Outline each Plasmodium malariae-infected red blood cell.
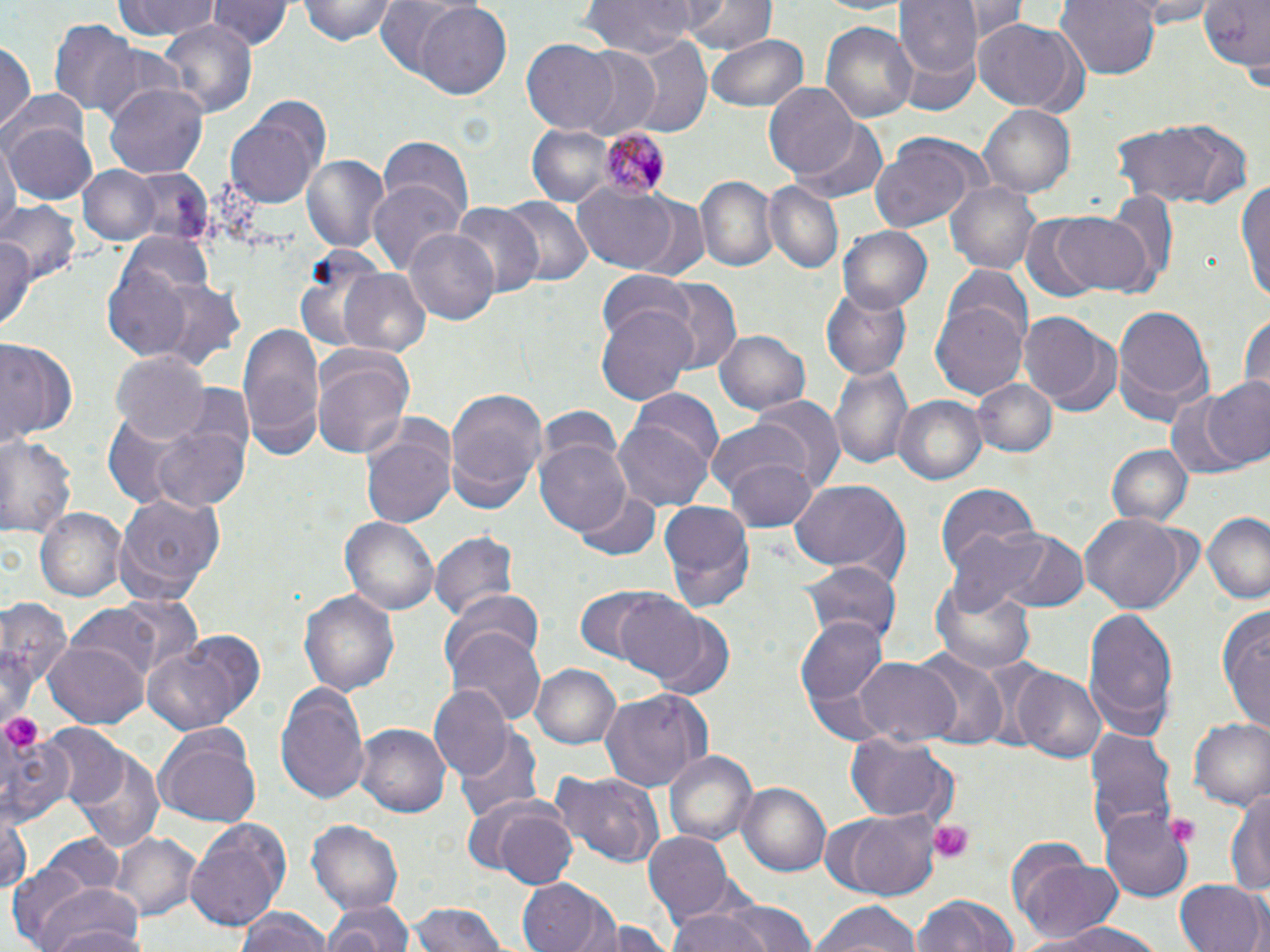
Approximate bounding boxes as [x1, y1, x2, y2] in pixels.
Plasmodium malariae-infected red blood cells: [593, 129, 669, 200].

{
  "slide_level_diagnosis": "Plasmodium malariae",
  "image_size": "1270×952 pixels",
  "modality": "optical microscopy",
  "magnification": "1000x",
  "field_of_view": "one of a larger specimen",
  "preparation": "thin blood smear",
  "uninfected_red_blood_cell_locations": "approximate bounding boxes as [x1, y1, x2, y2] in pixels: [110, 0, 223, 42], [210, 0, 289, 54], [296, 0, 398, 46], [372, 0, 472, 82], [580, 0, 702, 58], [680, 0, 775, 54], [800, 0, 916, 16], [894, 0, 981, 108], [959, 0, 1028, 39], [1055, 0, 1162, 79], [1117, 0, 1222, 25], [1197, 0, 1269, 78], [415, 4, 512, 101], [49, 17, 140, 114], [820, 18, 918, 126], [158, 21, 257, 118], [973, 21, 1090, 116], [628, 33, 713, 140], [706, 33, 809, 114], [1, 39, 35, 140], [522, 40, 622, 132], [563, 45, 665, 140], [105, 81, 209, 178], [766, 82, 863, 180], [227, 101, 330, 209], [978, 106, 1074, 197], [1110, 115, 1252, 212], [6, 120, 99, 204], [790, 123, 890, 203], [526, 124, 615, 206], [2, 135, 18, 243], [867, 135, 980, 234], [375, 140, 473, 230], [298, 153, 392, 257], [77, 164, 161, 244], [137, 164, 210, 241], [695, 176, 776, 272], [1235, 176, 1270, 305], [369, 180, 465, 279], [944, 180, 1040, 274], [761, 182, 844, 277], [571, 185, 686, 275], [1102, 187, 1179, 287], [5, 196, 80, 287], [500, 197, 591, 290], [626, 198, 711, 280], [448, 201, 543, 301], [1048, 209, 1157, 296], [1018, 216, 1103, 304], [838, 228, 932, 312], [404, 229, 499, 327], [0, 231, 38, 338], [291, 243, 392, 356], [103, 260, 200, 363], [338, 267, 432, 357], [944, 267, 1034, 353], [596, 273, 697, 350], [647, 275, 746, 375], [151, 280, 246, 371], [820, 284, 914, 379], [931, 301, 1027, 401], [1113, 303, 1214, 425], [596, 304, 697, 407], [1019, 311, 1114, 413], [1239, 311, 1269, 399], [237, 322, 325, 457], [714, 326, 813, 417], [0, 338, 76, 449], [310, 348, 415, 458], [111, 352, 208, 443], [831, 363, 914, 472], [973, 378, 1057, 460], [1199, 378, 1270, 471], [444, 386, 548, 514], [626, 390, 724, 482], [1163, 391, 1253, 482], [752, 393, 845, 491], [896, 395, 986, 485], [537, 403, 623, 489], [362, 418, 455, 530], [611, 419, 714, 512], [705, 419, 814, 503], [150, 420, 252, 515], [1, 434, 79, 540], [535, 438, 631, 538], [1105, 444, 1194, 529], [725, 454, 818, 532], [787, 478, 911, 584], [934, 481, 1041, 585], [575, 490, 661, 560], [114, 492, 228, 602], [659, 501, 757, 613], [37, 510, 126, 600], [1202, 513, 1269, 605], [1082, 514, 1186, 615], [340, 516, 438, 618], [989, 526, 1088, 613], [429, 528, 521, 622], [800, 558, 898, 645], [930, 571, 1039, 674], [298, 586, 402, 698], [573, 586, 680, 667], [448, 590, 545, 673], [610, 592, 713, 684], [1, 595, 72, 728], [64, 603, 182, 688], [1217, 604, 1269, 730], [1082, 606, 1180, 740], [645, 612, 738, 700], [799, 617, 888, 708], [447, 629, 545, 728], [44, 643, 147, 728], [140, 644, 248, 736], [915, 652, 1008, 749], [849, 657, 960, 745], [530, 664, 623, 750], [1010, 668, 1105, 763], [274, 682, 371, 804], [428, 686, 512, 782], [599, 687, 712, 791], [1188, 716, 1270, 811], [356, 724, 450, 819], [41, 725, 128, 813], [0, 726, 77, 829], [155, 726, 260, 824], [1085, 726, 1177, 848], [456, 730, 543, 824], [846, 734, 957, 823], [75, 749, 167, 855], [663, 750, 758, 848], [548, 769, 667, 867], [737, 782, 832, 879], [1226, 783, 1270, 896], [821, 807, 946, 899], [492, 808, 579, 890], [0, 812, 31, 898], [1099, 812, 1193, 901], [186, 818, 292, 931], [308, 820, 404, 919], [45, 832, 124, 898], [110, 832, 200, 920], [644, 832, 734, 923], [1013, 856, 1125, 944], [2, 866, 110, 948], [1174, 877, 1268, 952], [516, 878, 613, 952], [912, 892, 1020, 952], [39, 894, 147, 952], [717, 901, 818, 952], [319, 902, 412, 950], [808, 902, 922, 952], [405, 904, 511, 952], [664, 907, 777, 952], [234, 908, 333, 952], [582, 916, 674, 952], [1029, 920, 1165, 952]",
  "stain": "May-Grünwald-Giemsa",
  "platelet_locations": "approximate bounding boxes as [x1, y1, x2, y2] in pixels: [2, 716, 43, 749], [1168, 817, 1197, 846], [924, 819, 974, 862]"
}